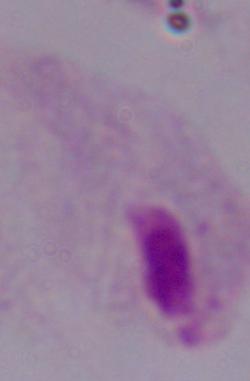
Summary:
  - Identification: trichomonad
  - Magnification: 1000x
  - Modality: photomicrograph